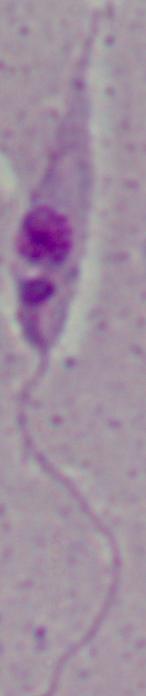

A Leishmania parasite is shown. Captured at 1000x magnification. Micrograph.